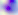

{
  "magnification": "400x",
  "modality": "micrograph",
  "identification": "Toxoplasma gondii"
}